Locate and identify every blood parasite.
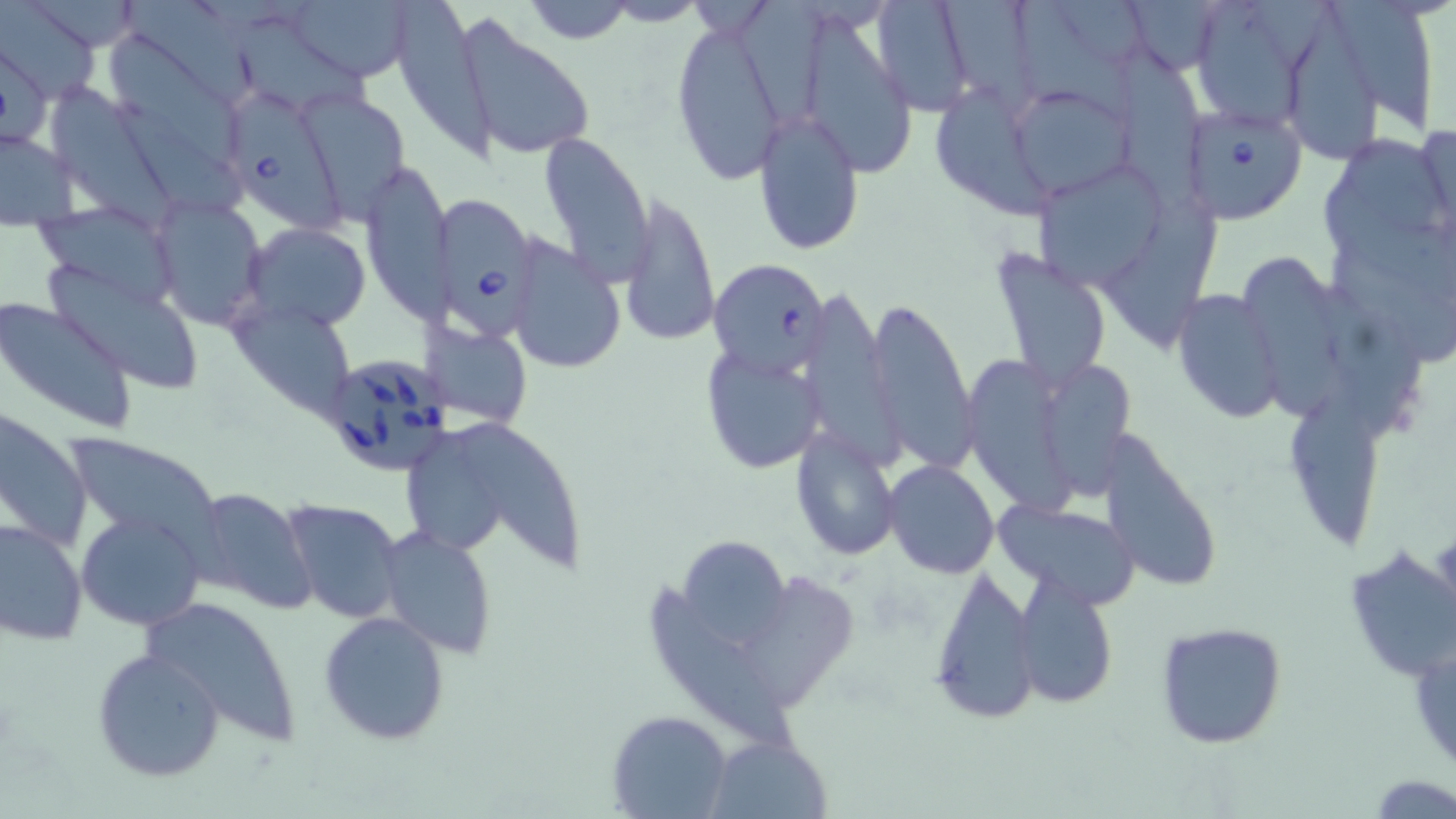

Approximate bounding boxes as [x1, y1, x2, y2] in pixels.
Babesia divergens-infected red blood cells: [229, 95, 352, 234], [1178, 102, 1307, 226], [438, 200, 543, 344], [708, 257, 831, 377], [321, 354, 454, 476].
No Plasmodium falciparum, Plasmodium ovale, Plasmodium malariae, Plasmodium vivax, or Trypanosoma brucei observed.

{
  "slide_level_diagnosis": "Babesia divergens",
  "stain": "May-Grünwald-Giemsa",
  "magnification": "1000x",
  "field_of_view": "one of a larger specimen",
  "preparation": "thin blood film",
  "modality": "optical microscopy",
  "image_size": "1456×819 pixels",
  "uninfected_red_blood_cell_locations": "approximate bounding boxes as [x1, y1, x2, y2] in pixels: [122, 0, 271, 108], [288, 0, 418, 80], [394, 0, 490, 158], [519, 0, 639, 46], [1014, 0, 1144, 122], [1120, 0, 1229, 76], [1198, 0, 1307, 130], [1, 1, 103, 102], [600, 1, 710, 26], [869, 1, 976, 114], [942, 1, 1041, 113], [1333, 1, 1433, 126], [735, 2, 835, 122], [1286, 13, 1380, 166], [669, 16, 791, 188], [806, 16, 922, 174], [242, 19, 374, 112], [457, 19, 596, 164], [109, 35, 248, 172], [1, 37, 52, 151], [1115, 44, 1206, 206], [1006, 85, 1135, 201], [54, 89, 184, 237], [941, 90, 1053, 221], [116, 93, 244, 220], [755, 107, 865, 255], [1419, 121, 1455, 232], [539, 131, 653, 281], [0, 132, 79, 225], [1346, 139, 1456, 233], [1029, 158, 1174, 292], [359, 160, 451, 327], [1319, 179, 1456, 292], [151, 195, 268, 331], [618, 196, 718, 346], [1109, 196, 1225, 347], [36, 204, 182, 310], [244, 222, 371, 333], [507, 238, 627, 373], [988, 249, 1112, 389], [1329, 251, 1456, 367], [1244, 257, 1345, 422], [47, 264, 207, 391], [800, 285, 893, 461], [1319, 286, 1430, 443], [1172, 289, 1288, 424], [863, 295, 975, 466], [0, 297, 137, 435], [226, 299, 360, 421], [431, 326, 531, 426], [700, 347, 828, 476], [962, 356, 1077, 518], [1041, 362, 1135, 508], [1295, 389, 1387, 550], [0, 410, 93, 555], [407, 423, 494, 555], [462, 426, 591, 572], [791, 426, 900, 561], [62, 433, 224, 551], [1103, 439, 1224, 595], [883, 460, 1000, 580], [187, 487, 318, 614], [280, 498, 407, 624], [998, 500, 1141, 607], [75, 510, 207, 632], [0, 518, 88, 646], [376, 525, 499, 658], [676, 532, 795, 649], [1342, 546, 1456, 687], [927, 565, 1040, 725], [1012, 572, 1119, 708], [747, 576, 864, 708], [650, 588, 792, 758], [143, 595, 304, 747], [319, 610, 450, 746], [1155, 621, 1288, 749], [1410, 639, 1456, 776], [92, 646, 226, 782], [608, 710, 729, 818], [706, 733, 831, 818], [1373, 775, 1455, 816]"
}